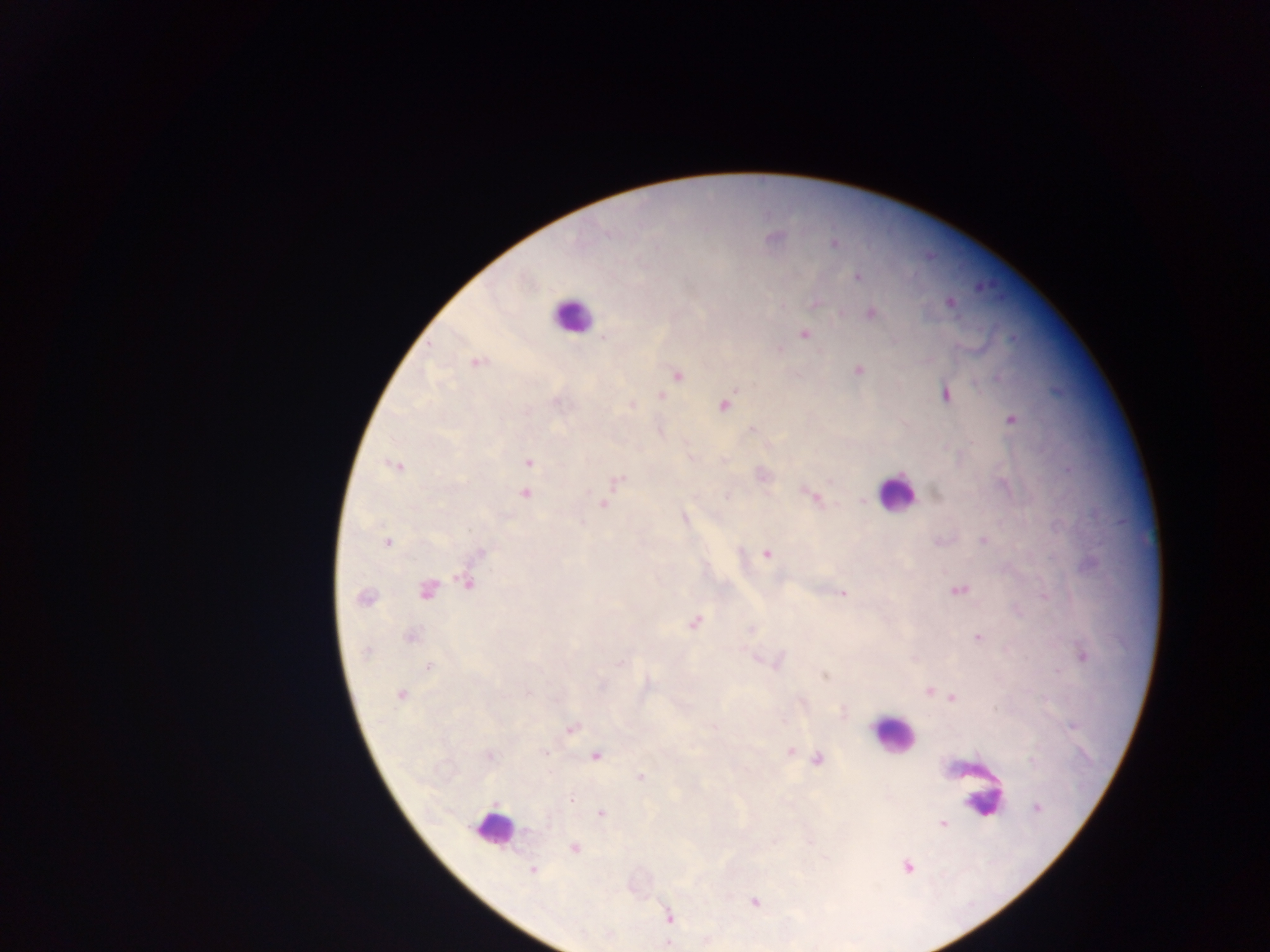
Approximate centers as (x, y) in pixels. Plasmodium parasite locations: (774, 237), (833, 245), (857, 276), (979, 289), (814, 302), (949, 302), (842, 311), (869, 312), (805, 335), (606, 338), (473, 362), (858, 370), (678, 376), (945, 395), (662, 396), (557, 403), (630, 404), (724, 405), (1010, 419), (752, 431), (691, 457), (724, 459), (528, 463), (394, 465), (828, 479), (615, 481), (525, 494), (815, 498), (863, 500), (603, 503), (685, 515), (470, 528), (984, 541), (387, 542), (479, 553), (766, 553), (470, 583), (427, 591), (958, 591), (844, 594), (1044, 596), (363, 599), (695, 624), (750, 629), (411, 635), (978, 638), (367, 652), (1083, 656), (756, 658), (620, 662), (779, 662), (429, 667), (825, 676), (400, 693), (528, 693), (945, 695), (844, 712), (572, 728), (791, 750), (544, 752), (490, 755), (595, 756), (818, 758), (640, 780), (572, 798), (1038, 808), (944, 823), (575, 848), (909, 867), (531, 869), (754, 901), (671, 916), (668, 943). Leukocyte locations: (567, 316), (900, 495), (889, 737), (976, 783), (492, 831). Sample from Ghana. Image is 1270×952 pixels. Thick blood film. Mobile-phone photograph taken through the microscope. One field of view.